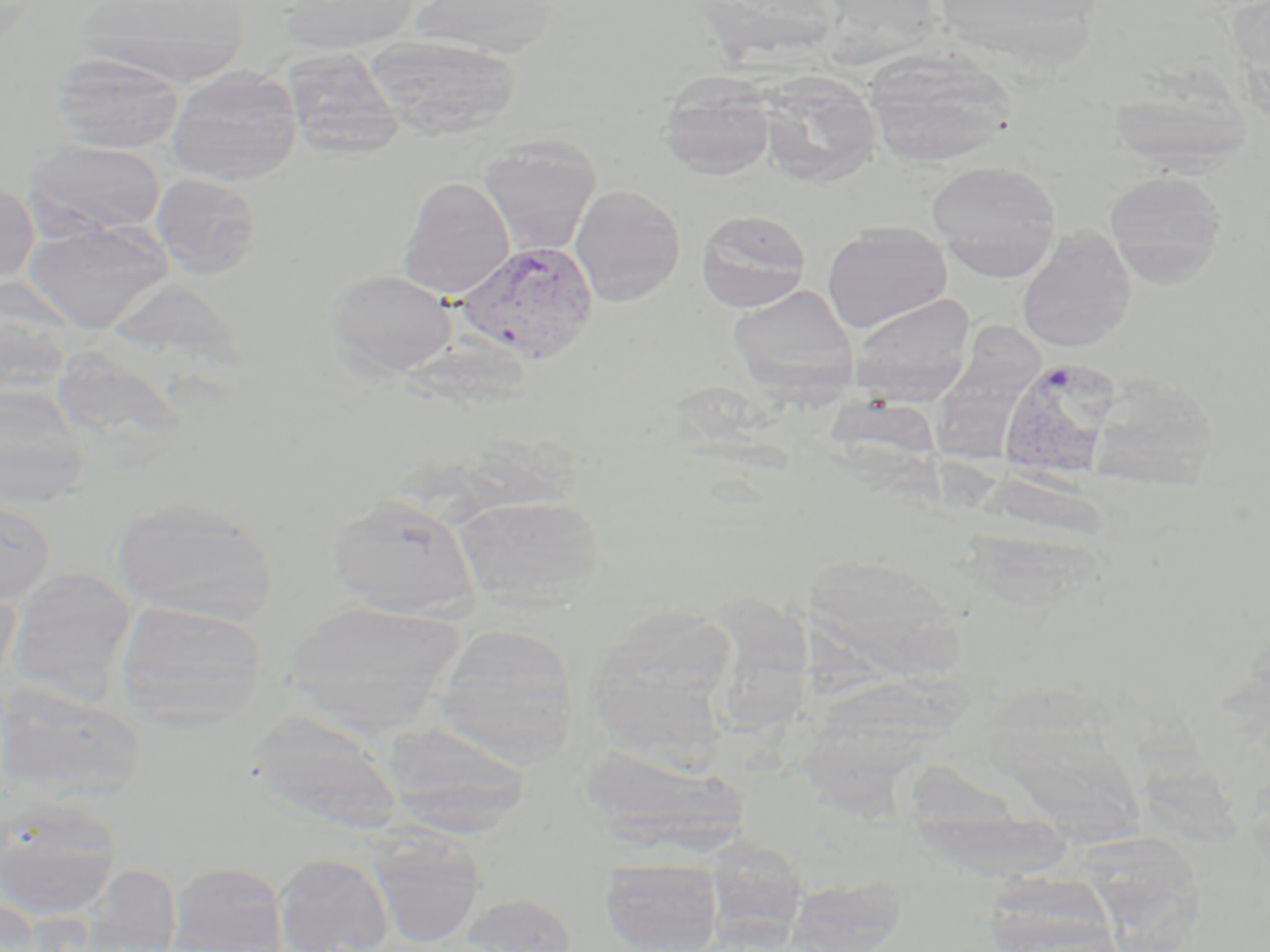
Approximate bounding boxes as (x1, y1, x2, y2) in pixels. Plasmodium vivax-infected red blood cell locations: (455, 240, 600, 366), (997, 356, 1122, 480). Uninfected red blood cell locations: (76, 0, 250, 87), (280, 0, 419, 56), (409, 0, 563, 57), (364, 35, 520, 139), (281, 48, 404, 159), (864, 50, 1019, 167), (52, 52, 184, 154), (166, 65, 302, 185), (657, 71, 776, 179), (755, 71, 882, 186), (1107, 74, 1256, 176), (478, 136, 601, 256), (25, 138, 168, 238), (926, 160, 1062, 269), (1104, 169, 1227, 284), (150, 173, 263, 278), (398, 177, 514, 299), (0, 183, 39, 289), (570, 185, 686, 306), (696, 209, 811, 312), (22, 218, 172, 333), (822, 222, 952, 333), (1016, 230, 1137, 353), (328, 270, 457, 379), (727, 285, 859, 396), (0, 288, 76, 407), (849, 294, 977, 400), (927, 325, 1044, 462), (1085, 373, 1220, 490), (0, 386, 90, 511), (328, 493, 480, 618), (455, 493, 605, 606), (0, 497, 55, 607), (111, 497, 277, 625), (799, 552, 967, 680), (6, 567, 137, 704), (0, 582, 20, 696), (730, 596, 883, 737), (116, 599, 266, 725), (284, 600, 465, 723), (585, 607, 742, 748), (434, 624, 579, 763), (990, 673, 1149, 853), (797, 674, 966, 814), (0, 686, 145, 806), (266, 717, 406, 838), (377, 719, 533, 837), (578, 745, 747, 858), (907, 751, 1076, 887), (0, 797, 123, 922), (366, 831, 487, 948), (1090, 834, 1209, 952), (274, 852, 394, 952), (600, 858, 723, 952), (167, 861, 290, 952), (86, 864, 182, 952), (980, 864, 1113, 950), (784, 874, 907, 952), (458, 893, 577, 952), (1, 895, 44, 952). Slide-level diagnosis: Plasmodium vivax. 1000x magnification. Optical microscopy. One field of a larger specimen. Thin blood film. May-Grünwald-Giemsa stain. Image is 1270×952 pixels.